Classify this cell by malaria status.
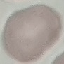

Uninfected.

capture: smartphone camera at the microscope eyepiece
stain: Giemsa
preparation: thin smear
image_type: automatically extracted cell patch, resized to 64 × 64 pixels